Report the malaria status of this cell.
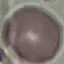

It is uninfected.

Summary:
  - Preparation: thin blood film
  - Stain: Giemsa
  - Image type: cell patch, automatically extracted from a larger field of view and resized to 64 × 64 pixels
  - Capture: smartphone through the microscope eyepiece